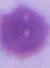

identification = erythrocyte
magnification = 1000x
modality = photomicrograph